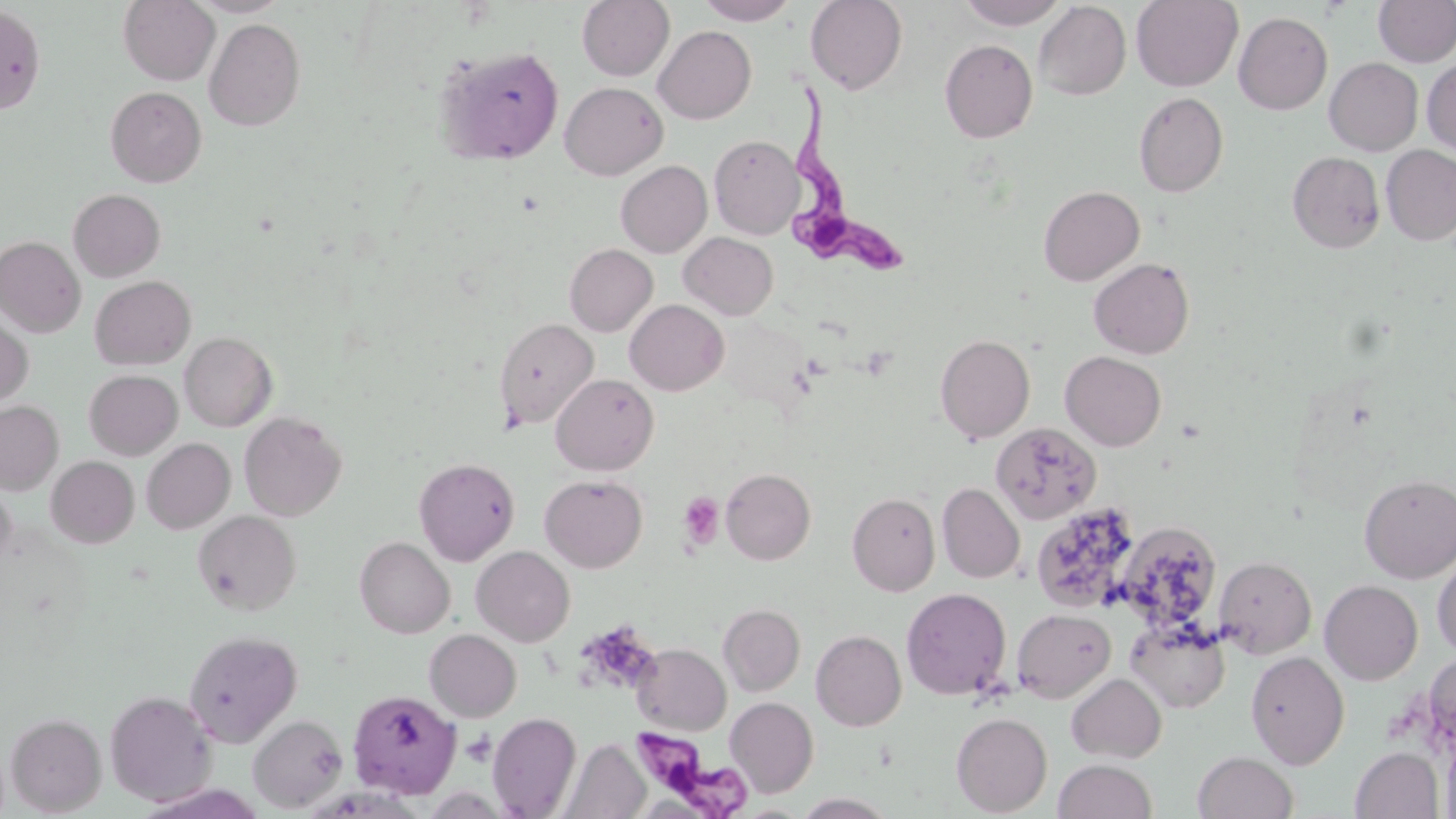

slide-level diagnosis = Trypanosoma brucei
uninfected red blood cell locations = approximate bounding boxes as (x1,y1)-(x2,y2) corner pairs in pixels: (118,0)-(219,85), (188,0)-(291,17), (577,0)-(674,81), (695,0)-(799,25), (805,0)-(908,95), (956,0)-(1068,29), (1131,0)-(1243,91), (1374,0)-(1456,67), (1034,2)-(1131,100), (0,4)-(46,114), (1234,11)-(1333,115), (204,18)-(305,131), (653,26)-(756,124), (939,39)-(1038,143), (436,45)-(564,166), (1324,57)-(1423,155), (1422,57)-(1456,157), (559,82)-(667,180), (105,86)-(206,187), (1134,92)-(1228,198), (710,135)-(803,239), (1381,145)-(1456,245), (1288,151)-(1385,253), (616,160)-(712,257), (1038,185)-(1144,285), (68,188)-(166,281), (680,232)-(778,319), (0,236)-(85,337), (564,244)-(657,336), (1089,257)-(1195,359), (90,275)-(196,370), (625,299)-(729,395), (0,314)-(33,407), (493,317)-(599,430), (179,332)-(277,431), (935,334)-(1035,443), (1060,351)-(1166,451), (84,369)-(182,459), (551,373)-(659,475), (0,401)-(63,494), (239,411)-(346,521), (991,422)-(1102,524), (142,438)-(235,534), (46,456)-(139,548), (414,457)-(520,566), (721,467)-(815,564), (540,474)-(648,572), (1359,474)-(1456,582), (0,480)-(16,572), (937,483)-(1025,583), (847,492)-(940,596), (1031,502)-(1139,614), (192,510)-(302,615), (1116,521)-(1223,632), (354,536)-(455,638), (471,545)-(575,647), (1432,553)-(1456,657), (1213,555)-(1316,658), (1320,580)-(1423,685), (901,587)-(1012,700), (719,603)-(805,696), (1012,608)-(1116,702), (1126,618)-(1230,713), (424,629)-(521,722), (183,630)-(303,746), (811,630)-(907,731), (632,643)-(731,735), (1245,650)-(1349,768), (1067,673)-(1167,763), (347,689)-(461,800), (104,690)-(218,806), (725,697)-(819,797), (5,712)-(106,816), (488,712)-(581,818), (952,712)-(1053,816), (249,714)-(348,812), (1441,730)-(1456,819), (561,738)-(650,819), (1350,747)-(1443,818), (1193,750)-(1298,819), (1053,759)-(1157,819), (794,793)-(896,818)
Trypanosoma brucei locations = approximate bounding boxes as (x1,y1)-(x2,y2) corner pairs in pixels: (790,82)-(916,279), (635,734)-(755,816)
modality = light microscopy
magnification = 1000x
platelet locations = approximate bounding boxes as (x1,y1)-(x2,y2) corner pairs in pixels: (678,491)-(725,550), (462,732)-(496,767)
stain = May-Grünwald-Giemsa
preparation = thin blood smear
field of view = one of a larger specimen
image size = 1456×819 pixels